Identify the blood parasite species.
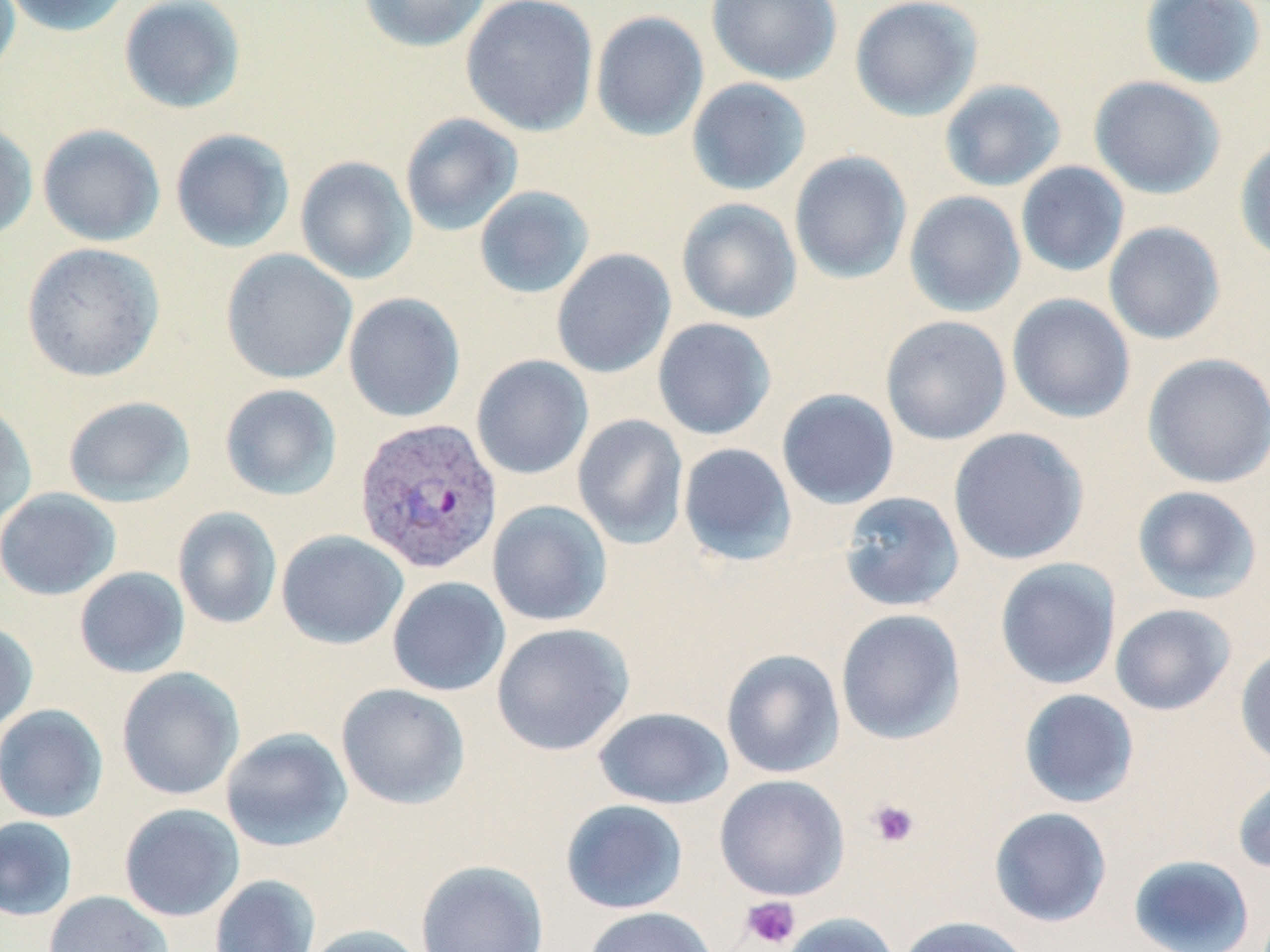
Plasmodium vivax.

Approximate bounding boxes as [x1, y1, x2, y2] in pixels. Platelet locations: [866, 798, 920, 848], [740, 896, 801, 949]. Uninfected red blood cell locations: [0, 0, 21, 82], [2, 0, 133, 37], [118, 0, 246, 114], [357, 0, 493, 53], [461, 0, 598, 136], [706, 0, 843, 85], [850, 0, 983, 121], [1140, 0, 1267, 89], [590, 10, 709, 141], [1089, 75, 1226, 200], [686, 78, 811, 196], [939, 79, 1067, 192], [400, 113, 523, 236], [0, 119, 38, 241], [37, 124, 165, 247], [170, 128, 295, 253], [1234, 138, 1270, 265], [789, 151, 912, 284], [295, 156, 417, 284], [1015, 161, 1129, 277], [474, 185, 595, 299], [904, 191, 1026, 317], [676, 198, 802, 324], [1103, 221, 1225, 345], [21, 242, 165, 382], [551, 248, 676, 380], [221, 249, 357, 384], [343, 292, 465, 423], [1006, 293, 1136, 424], [880, 316, 1011, 445], [652, 318, 776, 440], [1141, 352, 1270, 489], [471, 355, 593, 480], [220, 384, 342, 501], [776, 388, 899, 510], [63, 395, 196, 507], [0, 400, 37, 530], [572, 414, 689, 549], [948, 427, 1090, 565], [678, 442, 797, 566], [1131, 485, 1263, 603], [0, 488, 121, 600], [839, 491, 964, 612], [487, 500, 613, 627], [173, 507, 282, 629], [276, 530, 409, 650], [994, 558, 1122, 690], [74, 566, 190, 679], [387, 576, 511, 697], [1109, 603, 1236, 716], [835, 609, 966, 745], [0, 621, 38, 735], [491, 622, 634, 756], [1235, 647, 1270, 769], [720, 649, 845, 779], [116, 667, 244, 801], [336, 683, 471, 810], [1018, 688, 1140, 808], [0, 704, 108, 823], [593, 706, 734, 809], [220, 727, 353, 853], [1231, 773, 1270, 875], [714, 774, 849, 901], [560, 799, 689, 914], [119, 803, 244, 921], [989, 807, 1112, 928], [0, 816, 78, 921], [1128, 854, 1256, 952], [415, 860, 550, 952], [209, 874, 320, 952], [43, 890, 174, 952], [582, 906, 718, 952], [776, 912, 900, 952], [896, 915, 1034, 952], [301, 923, 428, 952]. Plasmodium vivax-infected red blood cell locations: [354, 417, 503, 576]. Image is 1270×952 pixels. May-Grünwald-Giemsa stain. Light microscopy. Thin blood film. One field of a larger specimen. 1000x magnification.